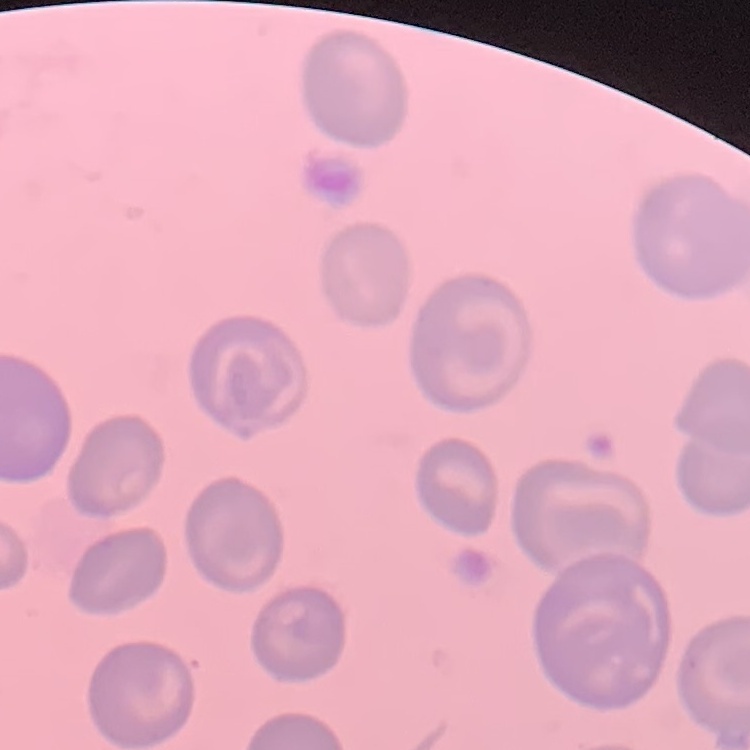
The red blood cells show no rouleaux formation. One tile cut from a larger photomicrograph. Thin peripheral smear. Field's or Giemsa stain.